Classify this cell by malaria status.
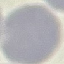

It is uninfected.

Thin blood film. Giemsa-stained preparation. Photographed with a smartphone camera at the microscope eyepiece. Automatically extracted cell patch, resized to 64 × 64 pixels.